Identify the blood parasite species.
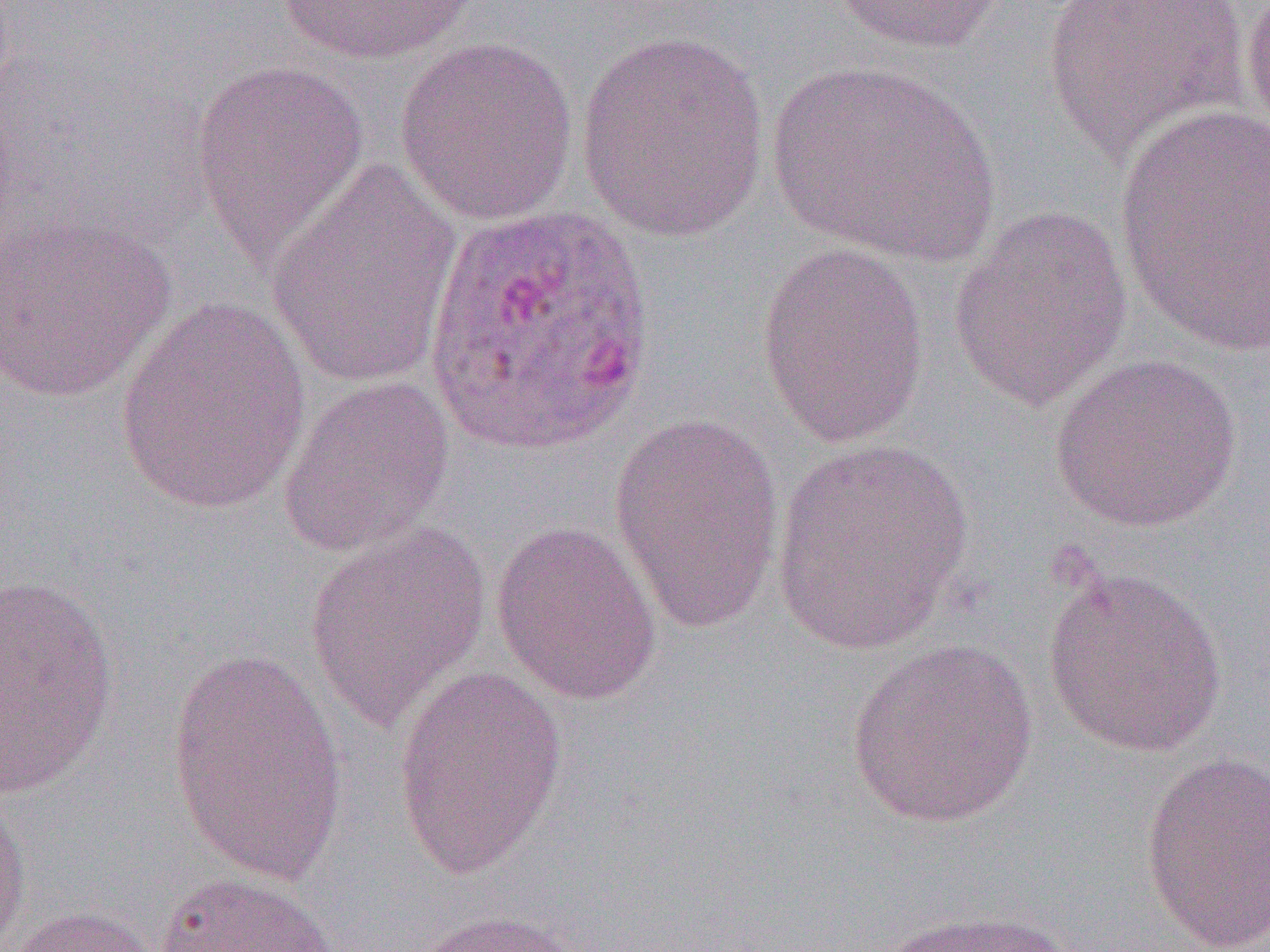
Plasmodium ovale.

modality = optical microscopy
preparation = thin blood smear
field of view = single
Plasmodium ovale-infected red blood cell locations = approximate bounding boxes as (x1, y1, x2, y2) in pixels: (423, 199, 654, 460)
image size = 1270×952 pixels
uninfected red blood cell locations = approximate bounding boxes as (x1, y1, x2, y2) in pixels: (275, 0, 484, 66), (827, 0, 1009, 57), (1039, 0, 1255, 164), (1240, 0, 1270, 145), (576, 30, 770, 243), (394, 36, 579, 227), (190, 58, 370, 268), (766, 61, 1000, 268), (1113, 105, 1270, 358), (267, 157, 462, 390), (947, 206, 1133, 412), (0, 210, 176, 403), (755, 241, 930, 448), (115, 299, 312, 516), (1049, 353, 1242, 534), (277, 375, 455, 557), (608, 412, 785, 634), (770, 438, 975, 656), (490, 519, 663, 706), (305, 522, 491, 732), (1042, 566, 1227, 758), (0, 571, 120, 797), (846, 638, 1039, 829), (166, 646, 349, 890), (392, 666, 568, 880), (1139, 751, 1270, 950), (0, 785, 32, 951), (155, 871, 341, 952), (5, 905, 167, 952), (873, 907, 1078, 952), (412, 909, 590, 952)
magnification = 1000x